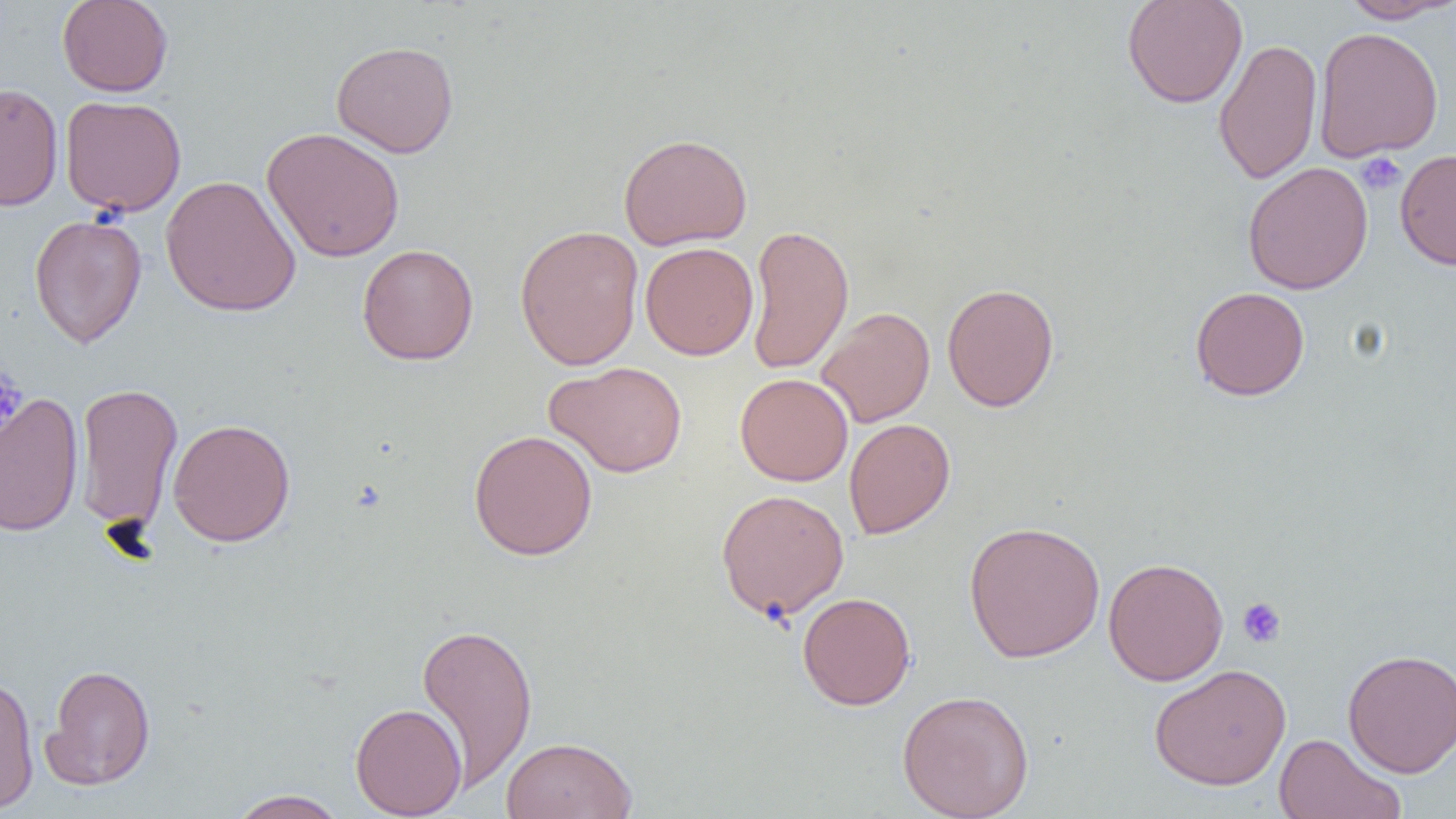

Summary:
  - Coordinate format: approximate bounding boxes as [x1, y1, x2, y2] in pixels
  - Platelet locations: [1355, 151, 1406, 196], [0, 367, 28, 438], [1237, 597, 1286, 649]
  - Uninfected red blood cell locations: [57, 0, 173, 97], [1122, 0, 1248, 109], [1336, 0, 1455, 24], [1313, 26, 1444, 162], [1212, 37, 1323, 185], [331, 40, 459, 158], [0, 83, 64, 212], [59, 95, 187, 217], [262, 127, 405, 263], [618, 132, 753, 251], [1395, 148, 1456, 270], [1242, 162, 1373, 295], [161, 174, 301, 318], [29, 214, 147, 348], [745, 223, 855, 375], [514, 224, 644, 370], [640, 242, 758, 360], [357, 243, 478, 364], [941, 282, 1060, 412], [1190, 286, 1310, 401], [816, 306, 935, 428], [545, 361, 687, 478], [734, 372, 854, 486], [74, 382, 183, 536], [0, 391, 84, 538], [167, 418, 296, 547], [843, 418, 955, 539], [468, 429, 598, 561], [715, 488, 850, 622], [964, 520, 1105, 662], [1103, 557, 1229, 686], [797, 592, 916, 710], [415, 620, 538, 792], [1342, 648, 1456, 778], [43, 663, 156, 789], [1149, 663, 1291, 791], [0, 673, 39, 814], [896, 689, 1036, 819], [350, 702, 467, 817], [1273, 733, 1406, 819], [500, 736, 637, 819], [227, 789, 349, 818]
  - Slide-level diagnosis: negative for blood parasites
  - Image size: 1456×819 pixels
  - Modality: optical microscopy
  - Field of view: single
  - Magnification: 1000x
  - Preparation: thin blood film